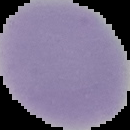

Malaria status: uninfected. Image is 130×130 pixels. Segmented cell region on a black background. From a thin blood smear.